Give the position of every leukocyte visible.
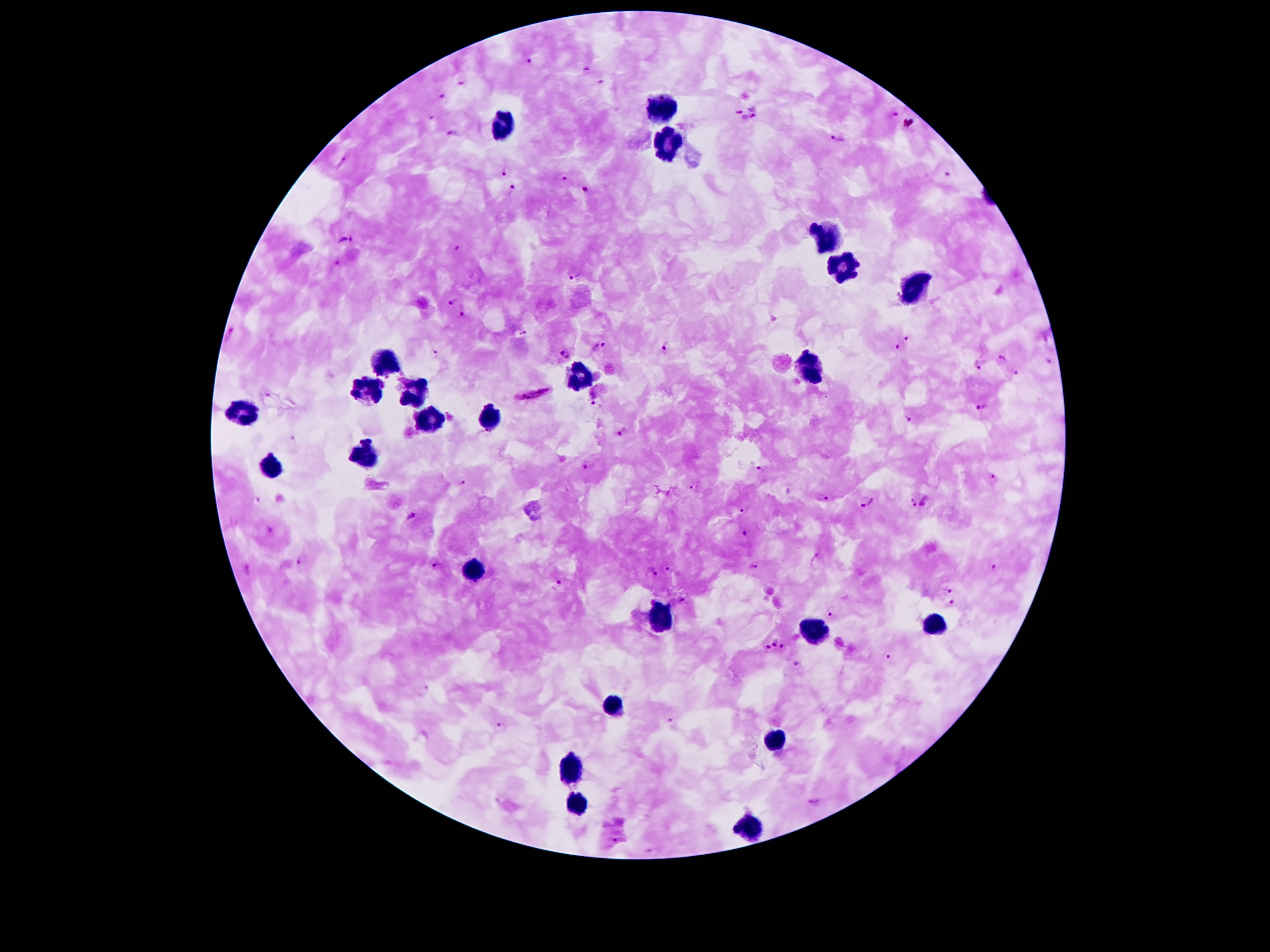
Approximate centers as [x, y] in pixels.
Leukocytes: [663, 107], [501, 125], [665, 145], [825, 235], [843, 269], [915, 287], [381, 357], [805, 369], [577, 371], [367, 387], [413, 397], [243, 413], [489, 413], [431, 421], [369, 455], [273, 467], [473, 571], [657, 619], [935, 625], [815, 631], [611, 707], [775, 739], [567, 773], [575, 807], [747, 829].

Malaria parasite locations: [530, 59], [588, 69], [460, 82], [601, 82], [442, 95], [753, 109], [738, 111], [896, 114], [748, 116], [450, 130], [836, 138], [502, 170], [948, 174], [565, 176], [513, 186], [586, 188], [346, 240], [457, 246], [339, 263], [574, 276], [454, 302], [463, 312], [230, 332], [524, 332], [907, 337], [666, 345], [599, 346], [897, 349], [566, 352], [434, 354], [1001, 360], [1049, 362], [979, 366], [1018, 372], [533, 392], [267, 394], [595, 404], [983, 407], [909, 420], [489, 432], [621, 432], [295, 439], [587, 467], [758, 468], [995, 477], [463, 483], [693, 487], [821, 497], [259, 499], [925, 500], [867, 502], [912, 504], [741, 509], [411, 516], [271, 527], [745, 533], [301, 559], [438, 566], [995, 566], [754, 567], [669, 569], [650, 574], [558, 584], [947, 589], [682, 599], [952, 603], [832, 610], [775, 641], [768, 647], [783, 647], [886, 655], [799, 663], [425, 689], [670, 719], [499, 727], [499, 800], [815, 801], [615, 841]. Patient malaria status: infected with Plasmodium falciparum. 100x magnification. Giemsa stain. Photographed through the microscope eyepiece with a smartphone camera. Single field of view. Thick peripheral-blood smear. Image is 1270×952 pixels.